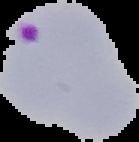
From a thin blood smear. Result: Plasmodium parasites identified. The area outside the segmented cell region is set to black. Image is 139×142 pixels.